State which parasite is depicted.
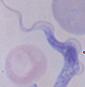

A trypanosome.

Summary:
  - Magnification: 1000x
  - Modality: photomicrograph